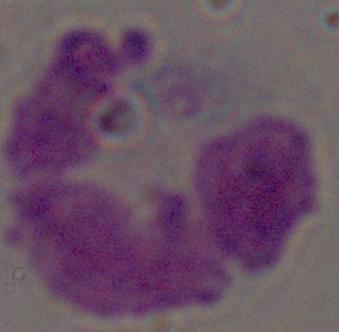 A white blood cell is shown. Micrograph. Captured at 1000x magnification.